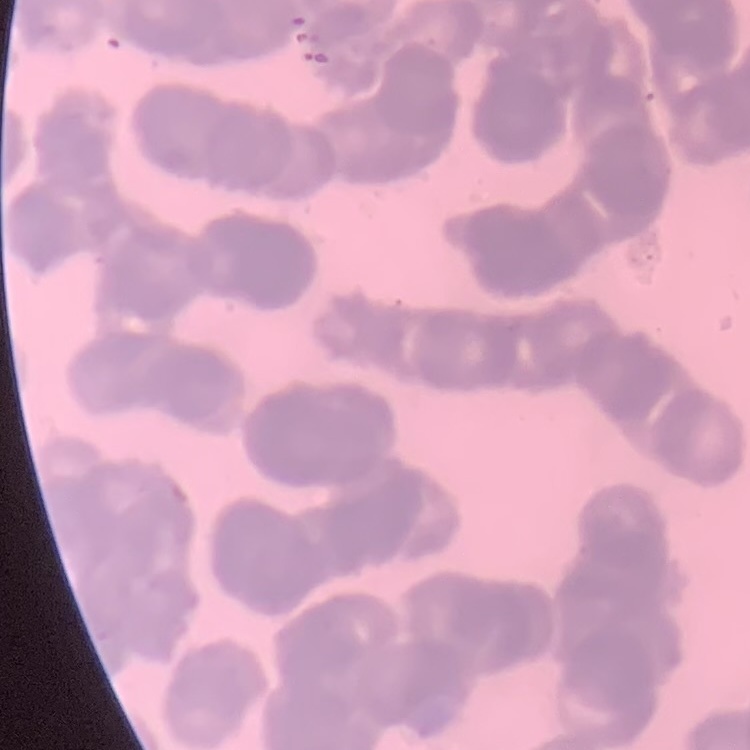

erythrocyte morphology = rouleaux formation
preparation = thin blood film
stain = Field's or Giemsa
image type = one tile cut from a larger photomicrograph